Look for Plasmodium parasites.
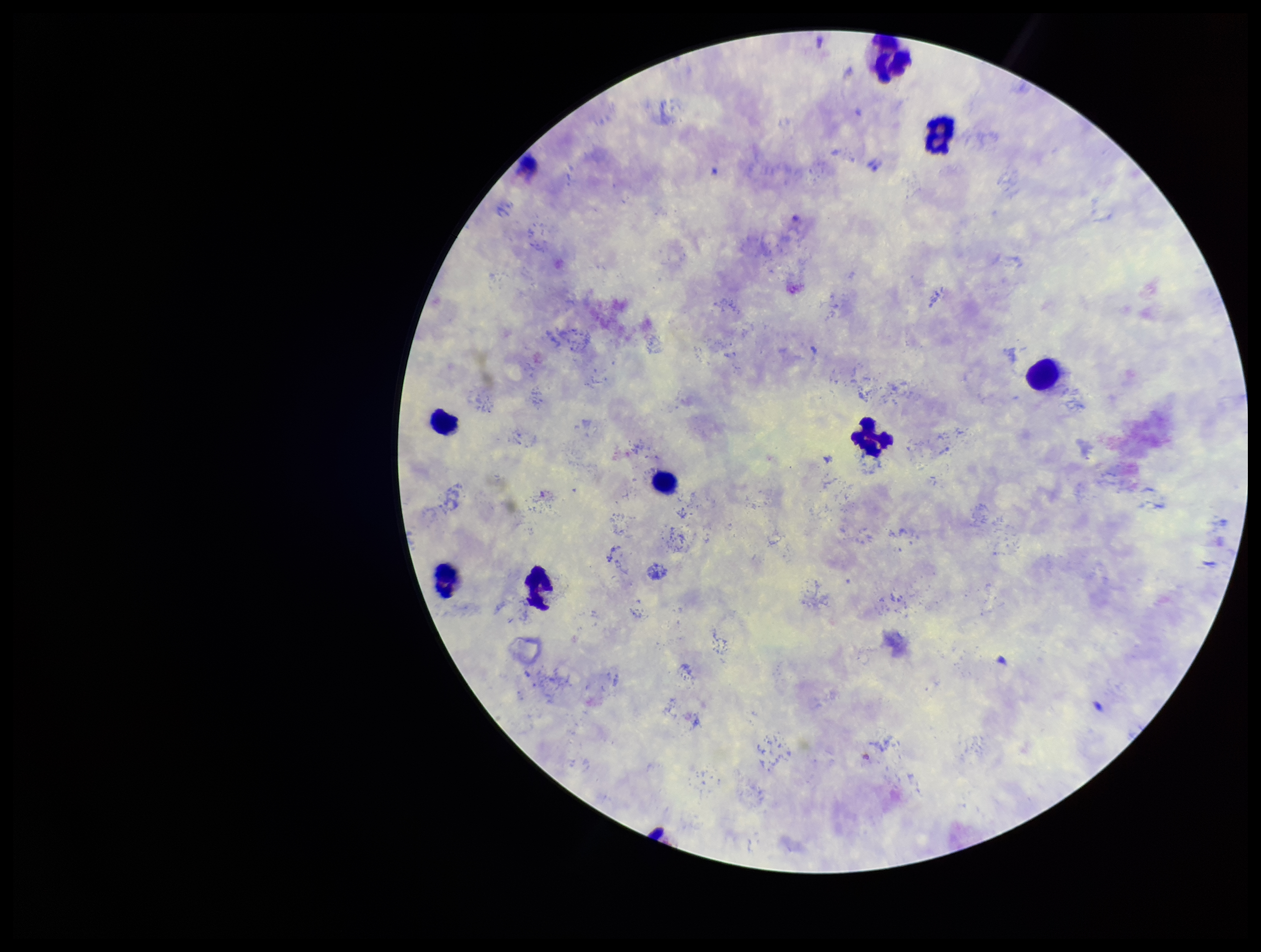
None detected.

Patient malaria status: infected. Stained with Giemsa. One field from this slide. Preparation: thick blood smear. Parasite count: 0. Photographed through the microscope eyepiece with a smartphone camera. Species reported for this patient: Plasmodium vivax. Leukocyte count: 9. Image is 1261×952 pixels.